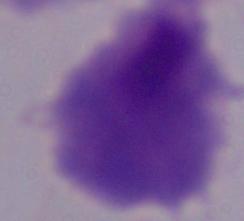

Summary:
  - Identification: trichomonad
  - Modality: photomicrograph
  - Magnification: 1000x